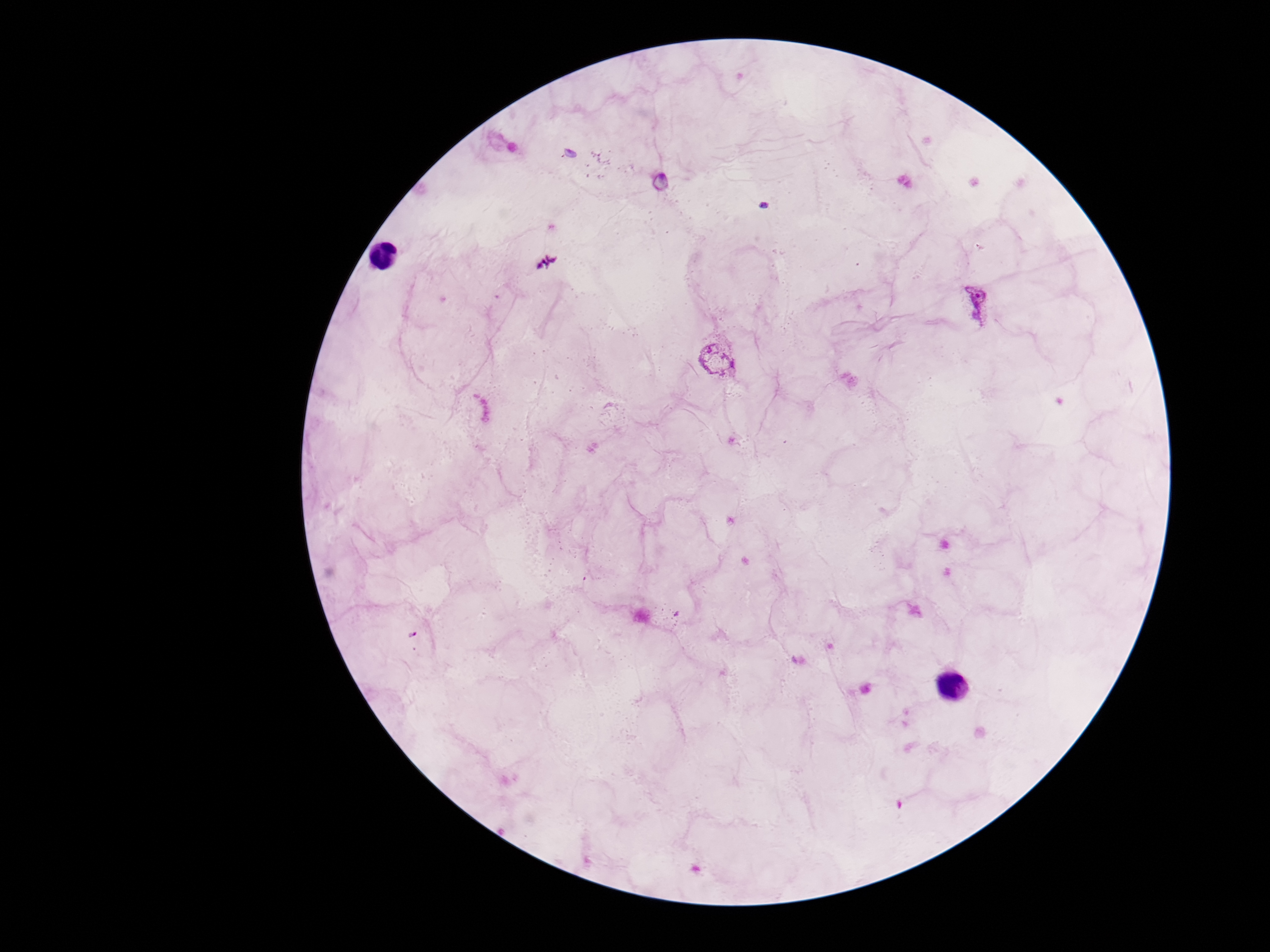

Approximate centers as {x, y} in pixels. Plasmodium parasite locations: {547, 261}, {977, 302}, {717, 355}, {414, 635}. Single field of view. Giemsa stain. Smartphone photograph taken through the microscope eyepiece. 100x magnification. Image is 1270×952 pixels. Patient malaria status: positive. Thick peripheral-blood smear.